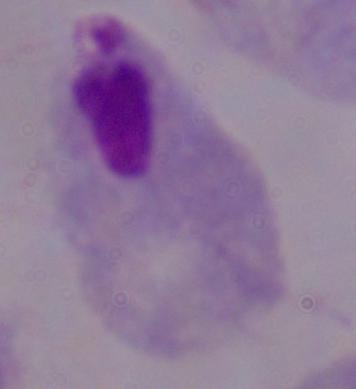
Summary:
  - Identification: trichomonad
  - Magnification: 1000x
  - Modality: photomicrograph